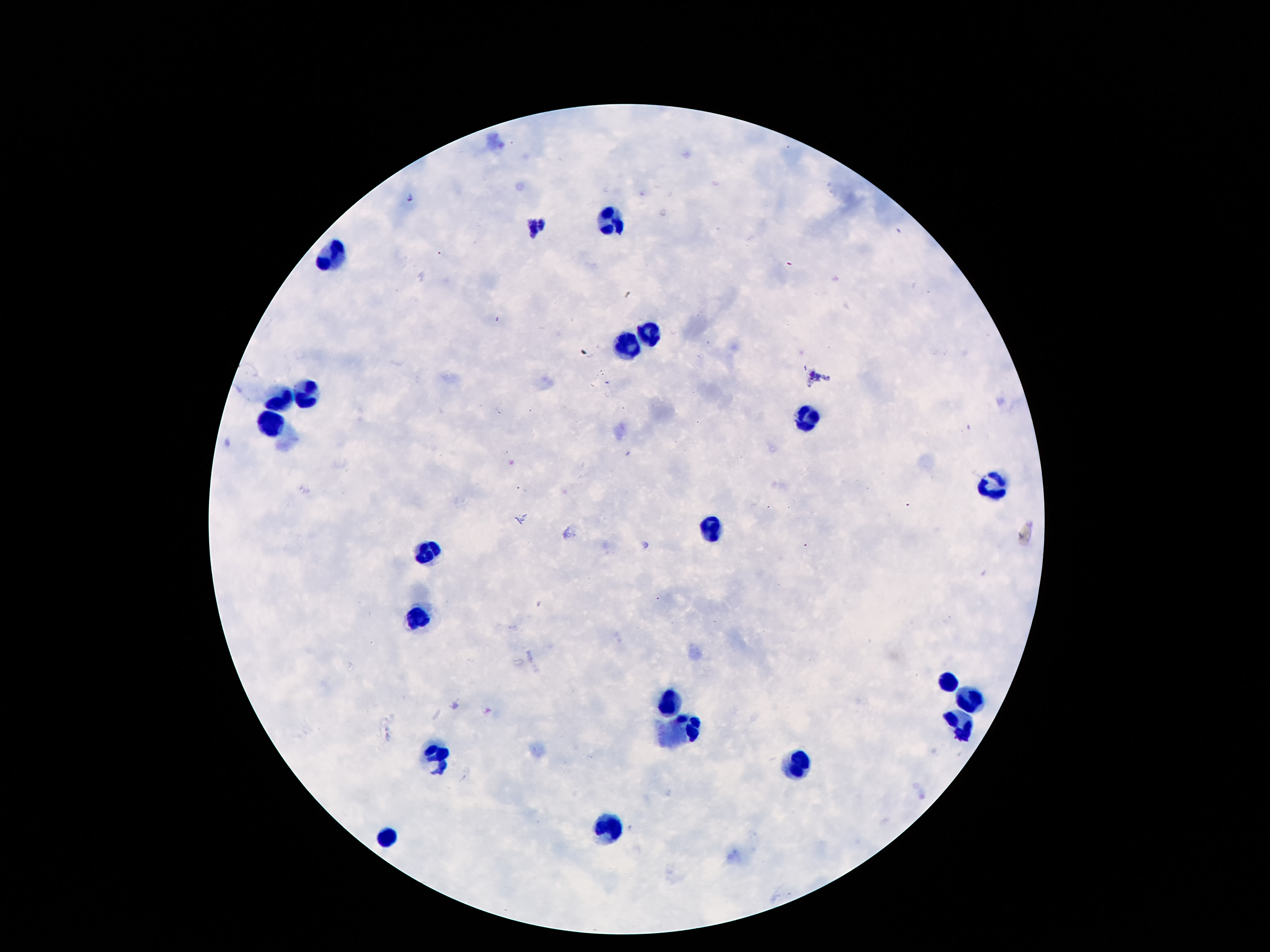
{
  "leukocyte_locations": "approximate centers as (x, y) in pixels: (611, 222), (332, 259), (650, 330), (629, 347), (306, 395), (280, 400), (807, 419), (271, 429), (994, 488), (712, 530), (424, 552), (415, 616), (951, 681), (672, 700), (971, 700), (960, 724), (693, 730), (439, 756), (796, 767), (611, 829), (387, 838)",
  "field_of_view": "single",
  "preparation": "thick blood smear",
  "capture": "smartphone camera through the microscope eyepiece",
  "magnification": "100x",
  "image_size": "1270×952 pixels",
  "stain": "Giemsa",
  "patient_malaria_status": "negative"
}